Assess for malaria.
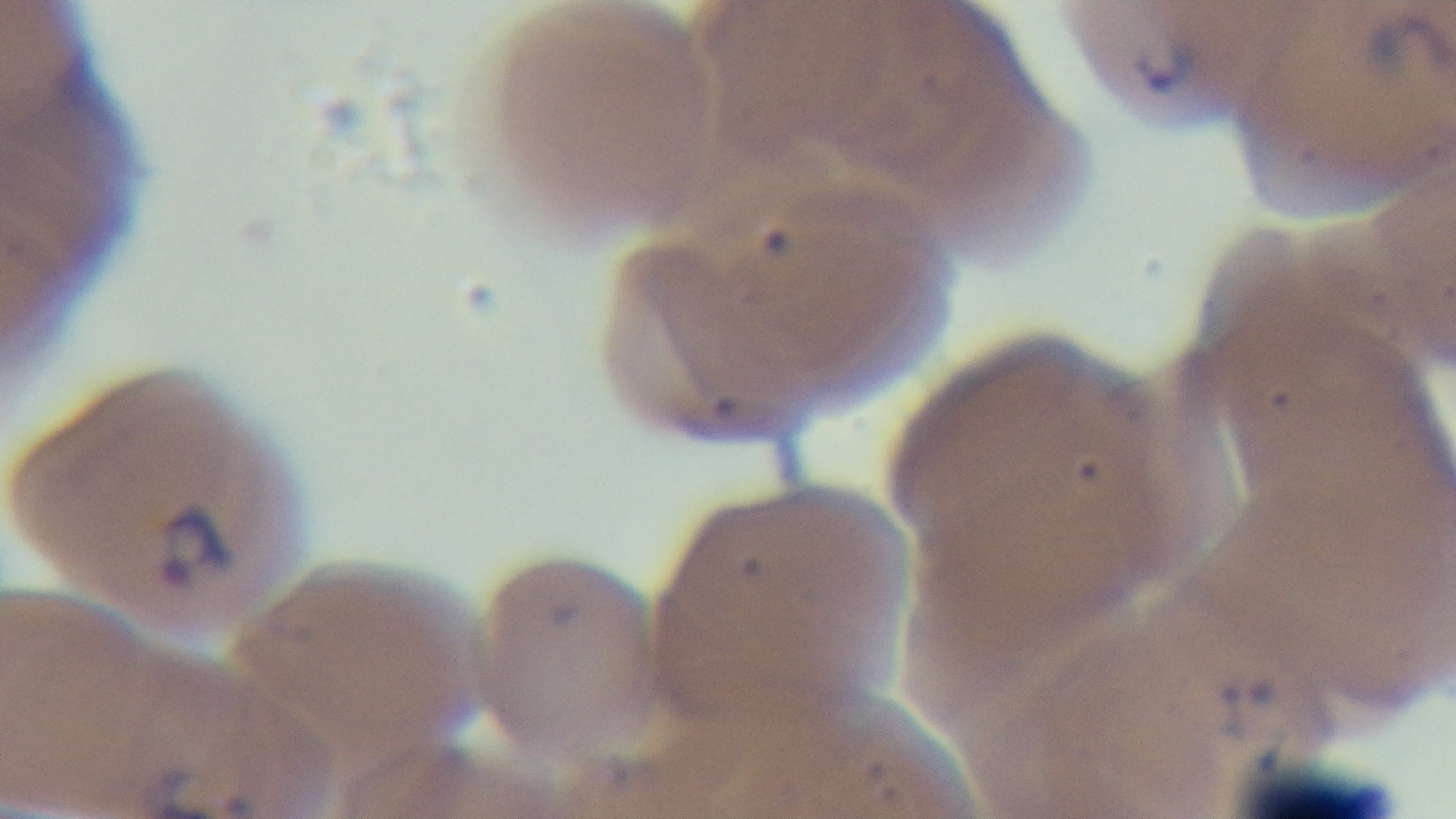

It is infected.

Giemsa-stained. One field from the slide. Oil-immersion objective, 100x. Captured with a mounted 4K digital camera. Photomicrograph. Preparation: thin blood film.